Locate the cells, classifying each as a parasitized red blood cell, an uninfected red blood cell, or a white blood cell.
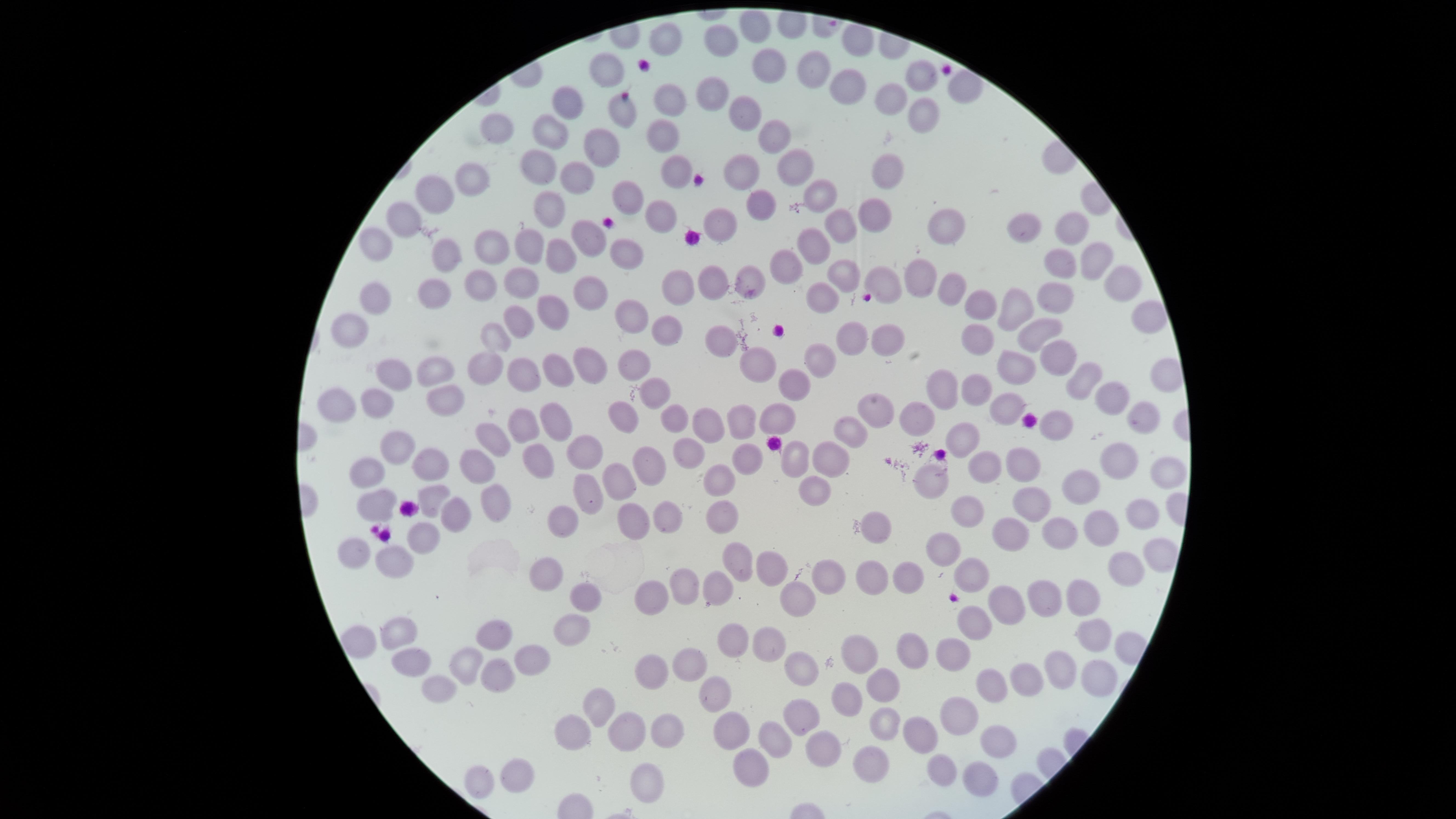
No parasitized red blood cells identified.
Approximate marker points as {x, y} in pixels.
Uninfected red blood cells: {754, 22}, {663, 39}, {726, 43}, {769, 63}, {604, 67}, {815, 67}, {923, 75}, {840, 85}, {710, 93}, {895, 96}, {670, 97}, {569, 99}, {622, 110}, {745, 110}, {915, 112}, {493, 128}, {550, 129}, {775, 130}, {664, 138}, {599, 150}, {539, 159}, {734, 160}, {885, 162}, {792, 163}, {669, 164}, {578, 174}, {475, 177}, {441, 190}, {821, 193}, {628, 194}, {754, 204}, {878, 206}, {551, 211}, {654, 214}, {404, 216}, {719, 223}, {939, 223}, {839, 224}, {1021, 229}, {1066, 232}, {593, 236}, {376, 243}, {807, 245}, {490, 247}, {551, 249}, {442, 250}, {523, 250}, {622, 252}, {1085, 260}, {786, 261}, {1060, 262}, {836, 272}, {884, 275}, {916, 276}, {742, 277}, {521, 280}, {476, 281}, {713, 282}, {957, 285}, {589, 286}, {1116, 286}, {675, 290}, {430, 294}, {1059, 297}, {375, 298}, {816, 300}, {983, 305}, {1016, 306}, {624, 312}, {548, 314}, {1153, 315}, {516, 322}, {1034, 328}, {354, 329}, {665, 330}, {972, 335}, {847, 337}, {494, 338}, {878, 338}, {717, 339}, {1051, 356}, {592, 358}, {553, 359}, {638, 361}, {819, 362}, {522, 363}, {759, 364}, {1019, 364}, {487, 366}, {430, 368}, {391, 372}, {791, 380}, {1079, 382}, {654, 384}, {948, 386}, {976, 387}, {444, 393}, {1110, 397}, {373, 400}, {336, 401}, {1003, 404}, {870, 407}, {557, 412}, {669, 412}, {772, 413}, {916, 415}, {622, 417}, {738, 417}, {1141, 417}, {1057, 422}, {529, 424}, {704, 428}, {849, 432}, {963, 433}, {482, 435}, {397, 436}, {592, 449}, {688, 452}, {829, 455}, {796, 456}, {1117, 459}, {1015, 460}, {420, 461}, {746, 461}, {986, 462}, {540, 463}, {470, 465}, {649, 467}, {364, 474}, {1161, 474}, {719, 477}, {925, 478}, {617, 479}, {582, 480}, {817, 481}, {1082, 485}, {431, 494}, {486, 498}, {377, 499}, {1027, 501}, {449, 509}, {969, 513}, {667, 514}, {723, 514}, {1141, 516}, {633, 518}, {560, 523}, {874, 523}, {1059, 531}, {1112, 532}, {416, 535}, {1006, 535}, {354, 546}, {946, 552}, {392, 555}, {740, 557}, {1154, 557}, {1117, 567}, {771, 570}, {870, 572}, {969, 573}, {550, 575}, {834, 577}, {906, 578}, {676, 581}, {715, 584}, {647, 590}, {1039, 593}, {1074, 593}, {796, 594}, {590, 598}, {1003, 599}, {973, 619}, {398, 630}, {564, 630}, {494, 634}, {1094, 634}, {359, 640}, {725, 640}, {912, 642}, {765, 648}, {853, 653}, {950, 655}, {528, 660}, {684, 661}, {410, 662}, {459, 662}, {647, 664}, {801, 664}, {1054, 669}, {493, 675}, {1026, 675}, {1091, 680}, {989, 683}, {439, 686}, {874, 688}, {712, 693}, {838, 698}, {599, 701}, {958, 709}, {797, 715}, {879, 727}, {666, 730}, {923, 731}, {573, 733}, {724, 733}, {624, 735}, {774, 735}, {994, 737}, {815, 744}, {748, 761}, {864, 761}, {517, 769}, {944, 772}, {982, 776}, {482, 778}, {642, 783}.
No white blood cells identified.

Image is 1456×819 pixels. Giemsa-stained preparation. Circular visible region. One field of view of the specimen. Photographed with a smartphone camera through the microscope eyepiece. Thin smear of blood.